Report the malaria status of this cell.
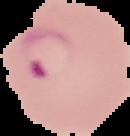

It is parasitized.

From a thin blood film. Image is 130×136 pixels. The area outside the segmented cell region is set to black.